Describe the morphology of the red blood cells.
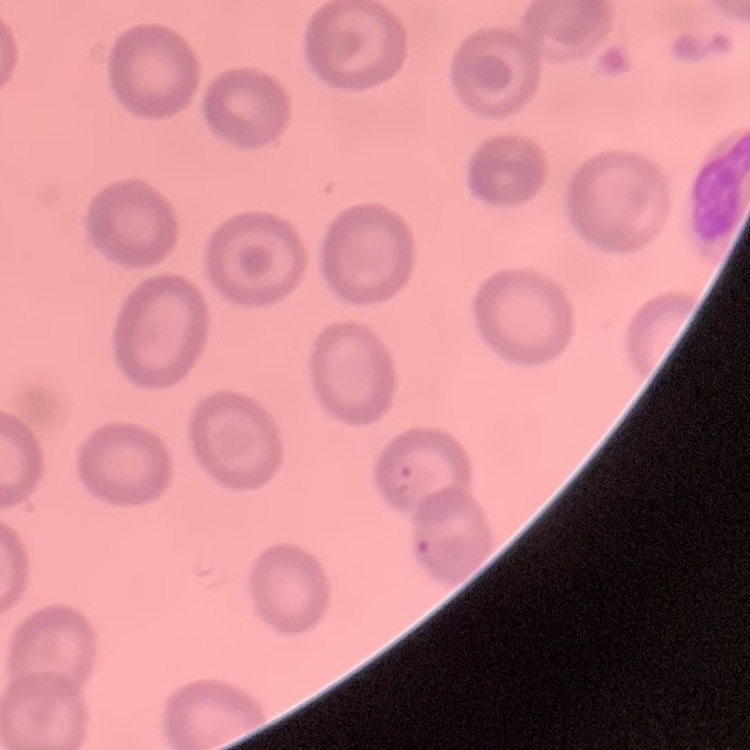

They show no rouleaux formation.

Summary:
  - Image type: one tile cut from a larger photomicrograph
  - Preparation: thin blood film
  - Stain: Field's or Giemsa